State which parasite is depicted.
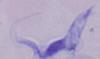

A trypanosome.

{
  "magnification": "1000x",
  "modality": "photomicrograph"
}